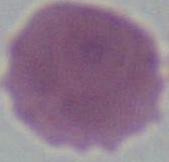

modality: micrograph
identification: erythrocyte
magnification: 1000x